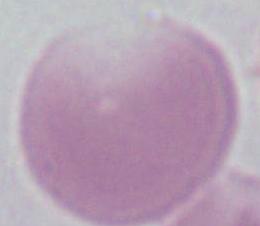

{
  "identification": "erythrocyte",
  "magnification": "1000x",
  "modality": "micrograph"
}